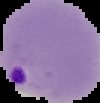
preparation: thin blood smear
image_size: 100×103 pixels
result: Plasmodium parasites identified
image_type: segmented cell region on a black background